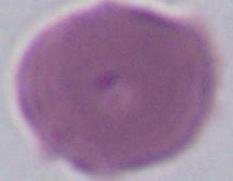
Micrograph. Captured at 1000x magnification. A red blood cell is seen.